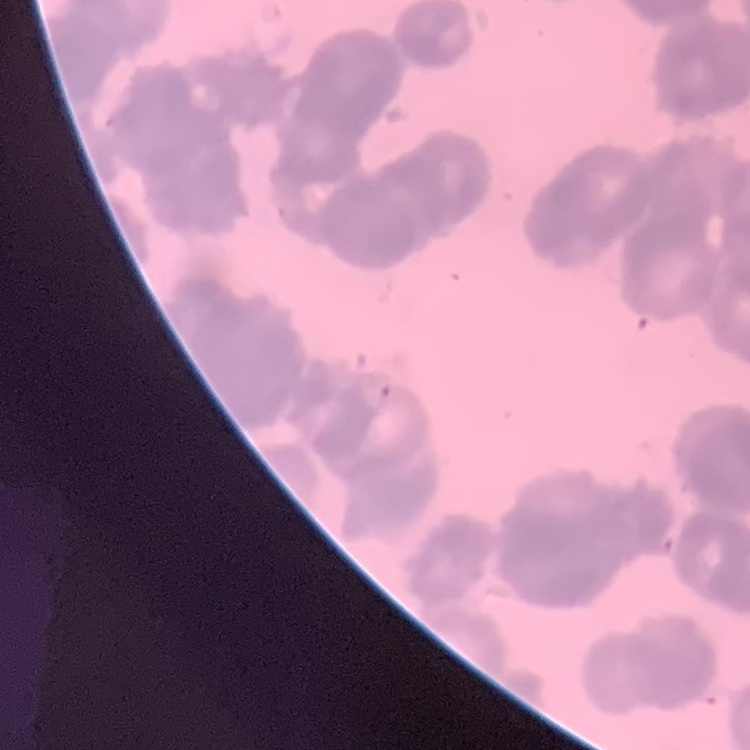

erythrocyte morphology = rouleaux formation
preparation = thin blood film
stain = Field's or Giemsa
image type = one tile cut from a larger photomicrograph